Identify the parasite.
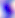

This is Toxoplasma gondii.

Summary:
  - Magnification: 400x
  - Modality: micrograph